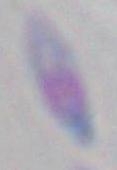
modality = micrograph
magnification = 1000x
identification = Toxoplasma gondii